Assess the morphology of the red blood cells.
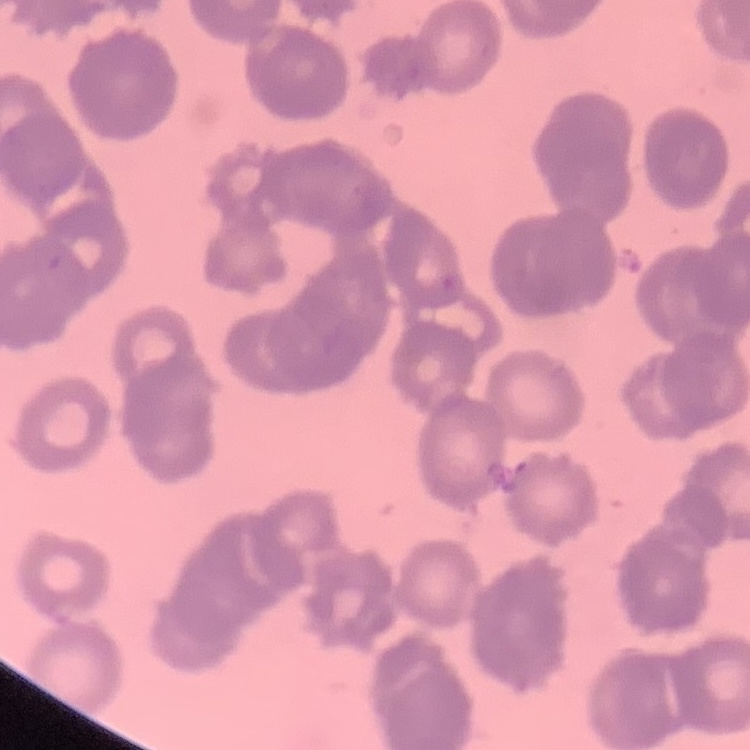
They show rouleaux formation.

preparation = thin blood film
stain = Field's or Giemsa
image type = square crop of a larger photomicrograph